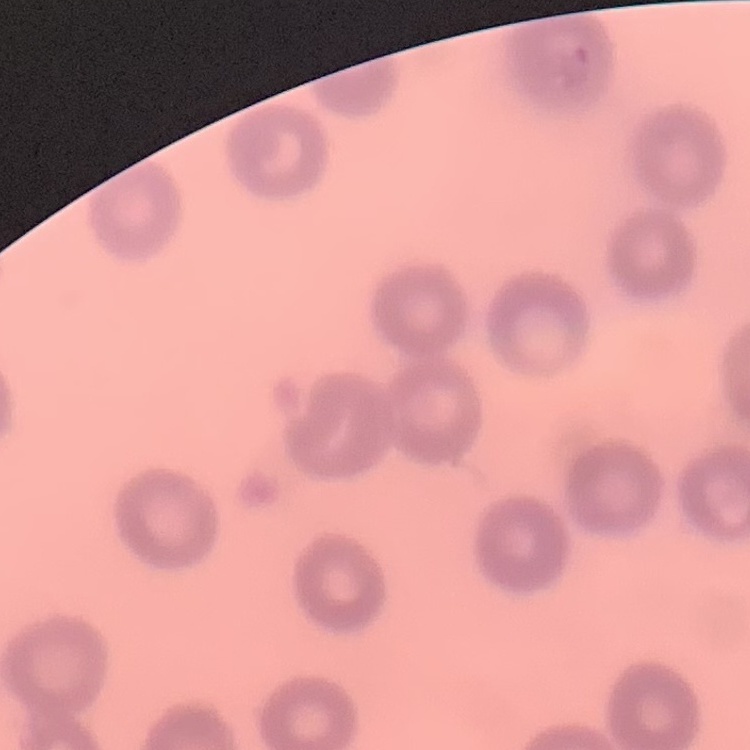

red blood cell morphology = no rouleaux formation
image type = square crop of a larger photomicrograph
stain = Field's or Giemsa
preparation = thin blood smear